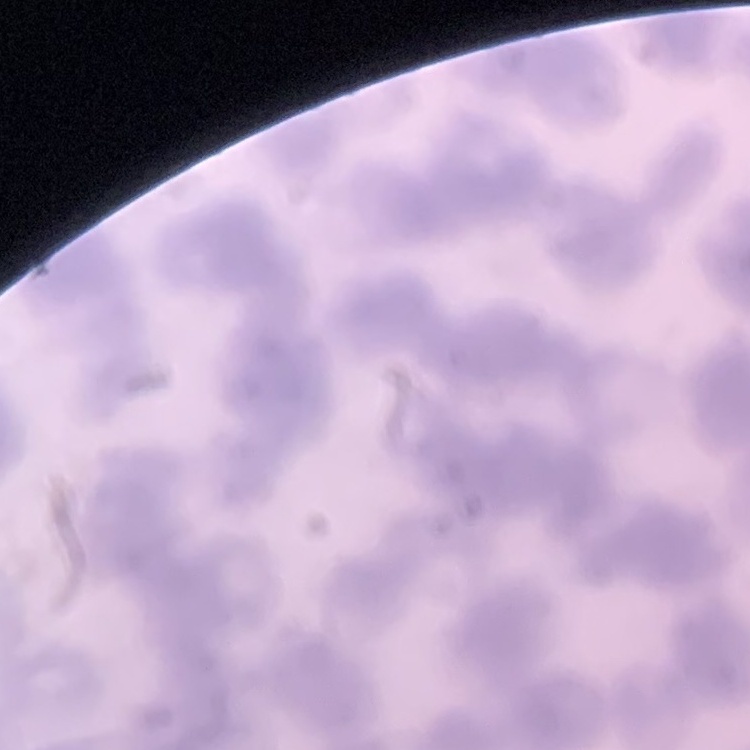
Summary:
  - Red blood cell morphology: rouleaux formation
  - Preparation: thin peripheral smear
  - Image type: square crop of a larger photomicrograph
  - Stain: Field's or Giemsa